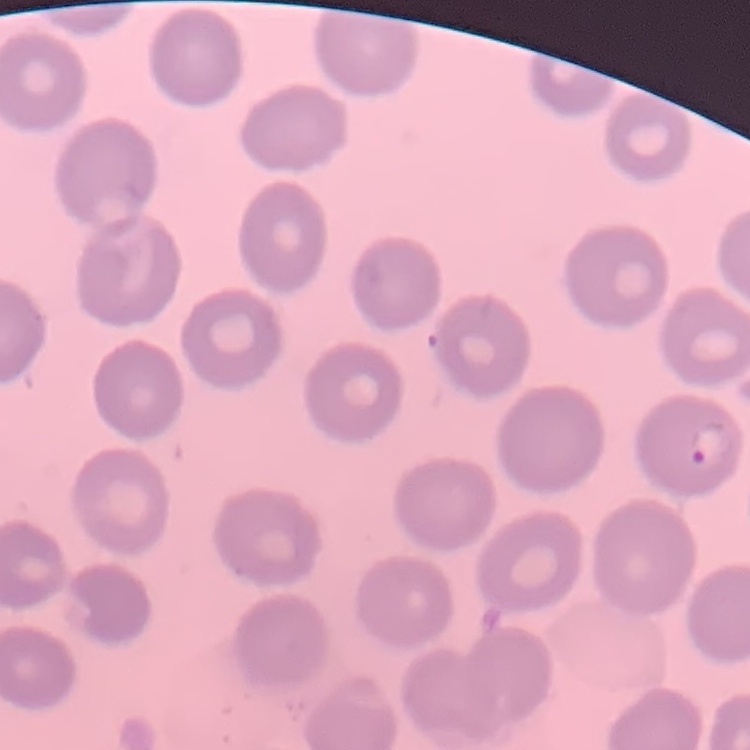
red_blood_cell_morphology: no rouleaux formation
preparation: thin blood smear
image_type: one tile cut from a larger photomicrograph
stain: Field's or Giemsa